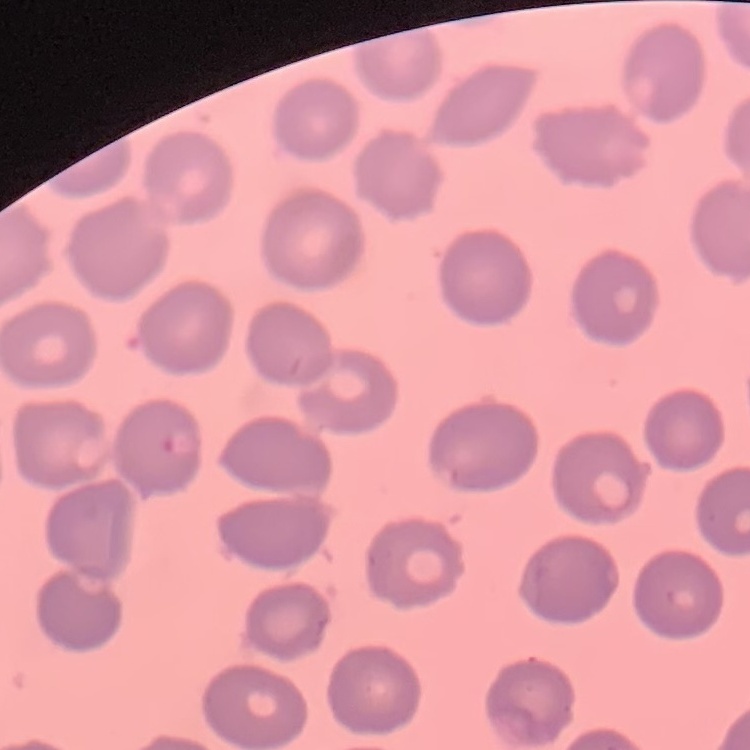 The erythrocytes show no rouleaux formation. Stained with either Field's or Giemsa. One tile cut from a larger photomicrograph. Thin peripheral smear.